Outline each blood parasite and name the species.
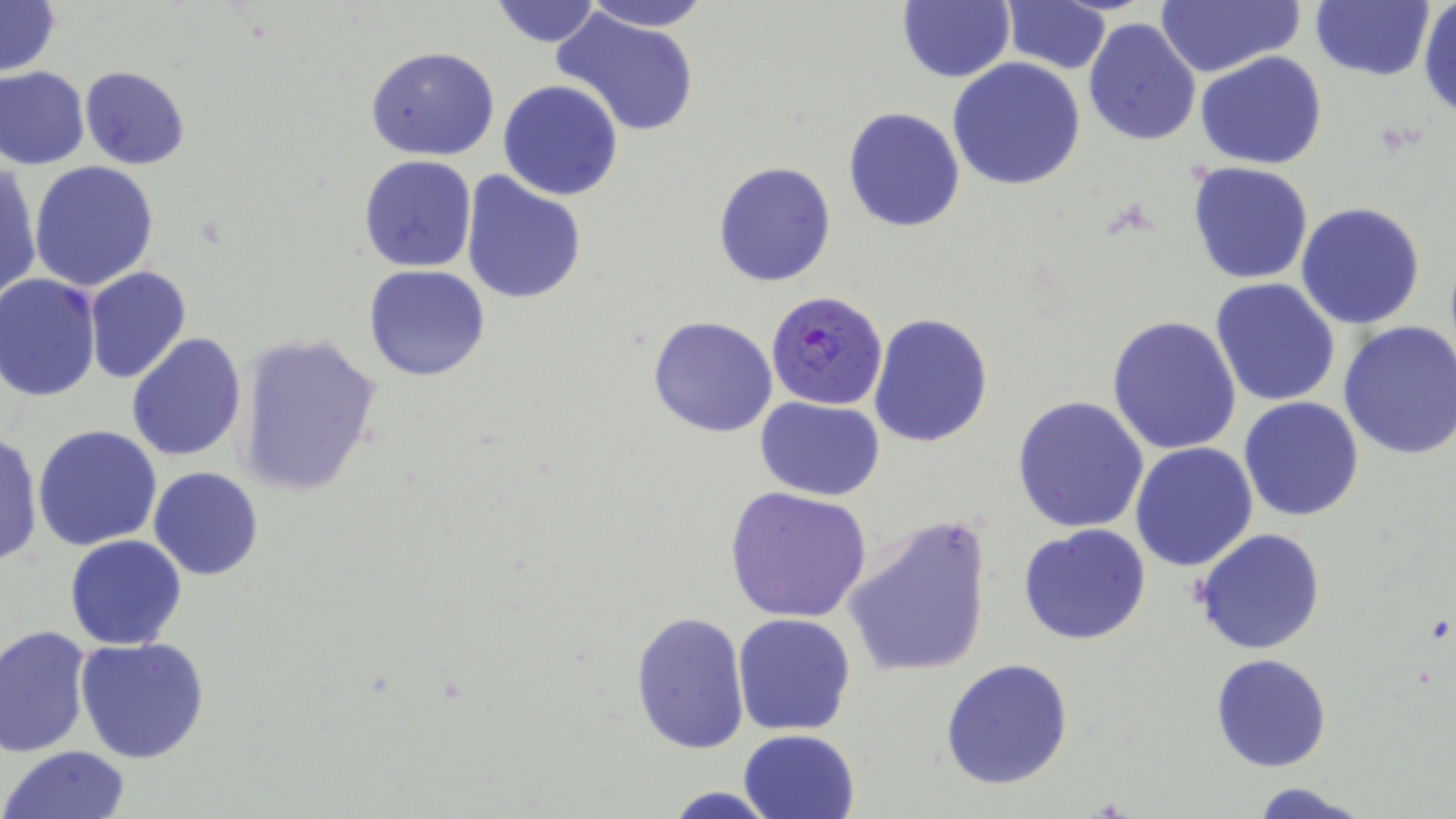

Approximate bounding boxes as (x1,y1)-(x2,y2) corner pairs in pixels.
Plasmodium falciparum-infected red blood cells: (764,290)-(887,410).
No Plasmodium ovale, Plasmodium malariae, Plasmodium vivax, Babesia divergens, or Trypanosoma brucei observed.

Uninfected red blood cell locations: (489,0)-(603,48), (575,0)-(716,32), (899,0)-(1014,82), (1151,0)-(1305,77), (1309,0)-(1434,82), (0,1)-(59,77), (1000,1)-(1113,74), (1418,1)-(1456,119), (555,10)-(701,137), (1081,17)-(1202,147), (366,46)-(499,161), (1196,52)-(1328,170), (947,57)-(1086,192), (0,66)-(89,170), (79,66)-(189,170), (498,80)-(625,201), (843,106)-(966,231), (358,156)-(477,273), (713,160)-(837,287), (28,161)-(159,291), (1187,161)-(1313,284), (0,163)-(40,306), (460,171)-(587,305), (1296,201)-(1427,330), (83,265)-(191,384), (363,265)-(491,382), (0,274)-(102,400), (1211,278)-(1341,407), (868,311)-(995,448), (647,314)-(778,438), (1107,314)-(1242,456), (1337,318)-(1456,460), (236,332)-(384,500), (127,333)-(247,462), (755,396)-(885,499), (1011,396)-(1149,533), (1239,396)-(1365,521), (33,425)-(162,551), (0,431)-(43,568), (1130,442)-(1259,572), (149,467)-(263,581), (723,485)-(872,623), (843,514)-(993,679), (1017,523)-(1153,645), (1192,528)-(1327,654), (65,534)-(187,649), (629,610)-(751,756), (732,613)-(858,736), (1,626)-(90,756), (74,636)-(209,762), (1210,654)-(1331,772), (940,658)-(1073,790), (738,730)-(859,819), (4,745)-(133,819), (1248,780)-(1376,819), (664,786)-(775,819). Slide-level diagnosis: Plasmodium falciparum. 1000x magnification. Thin blood smear. Image is 1456×819 pixels. Optical microscopy. May-Grünwald-Giemsa stain. Single field of view.